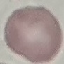
malaria status = uninfected
image type = cell patch, automatically extracted from a larger field of view and resized to 64 × 64 pixels
capture = smartphone camera at the microscope eyepiece
preparation = thin blood film
stain = Giemsa